Locate every blood parasite and identify its species.
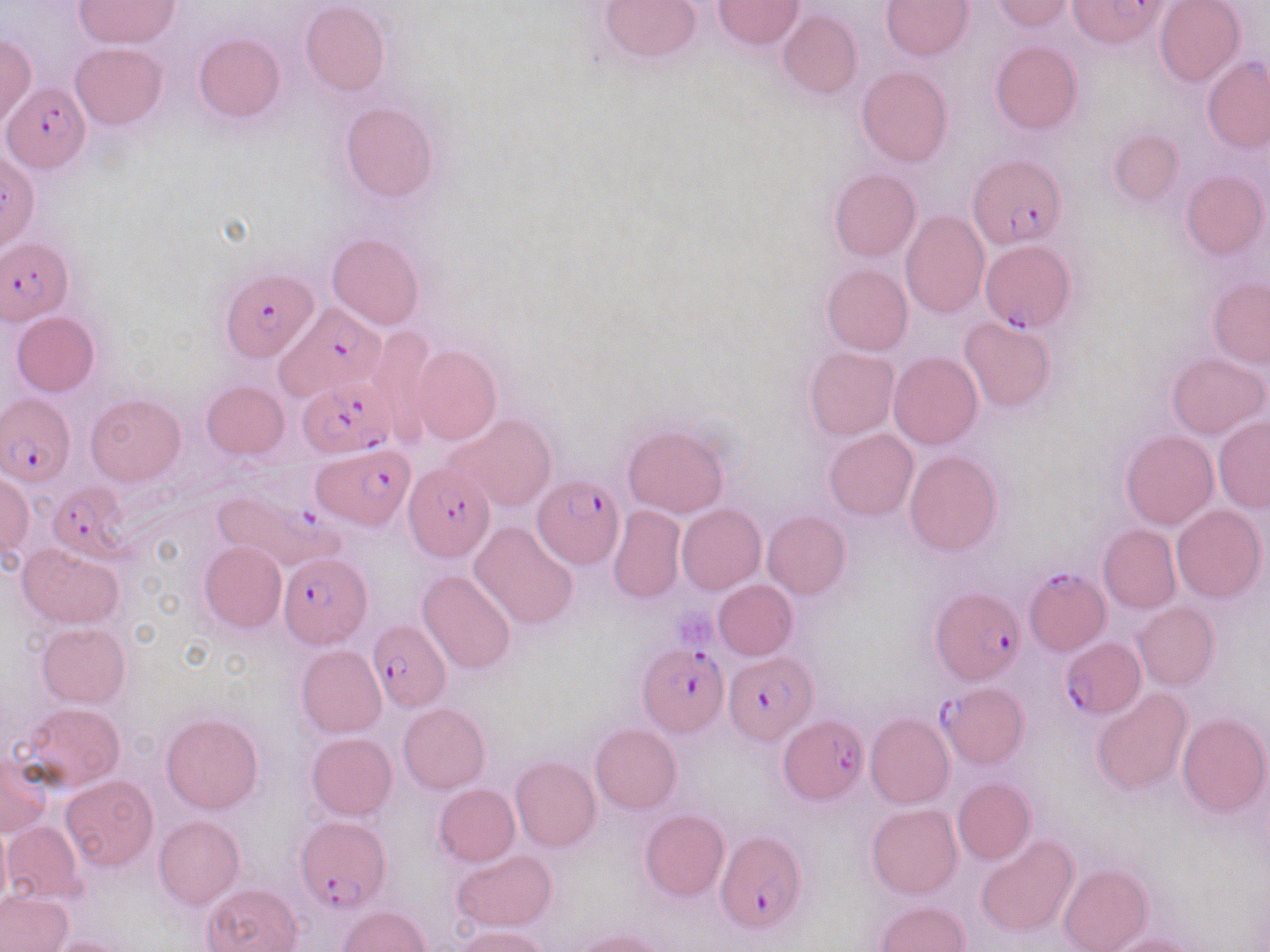
Approximate bounding boxes as [x1, y1, x2, y2] in pixels.
Plasmodium falciparum-infected red blood cells: [1068, 0, 1169, 46], [5, 81, 89, 174], [968, 151, 1067, 251], [0, 238, 74, 323], [980, 240, 1075, 331], [221, 269, 317, 360], [271, 304, 384, 400], [297, 378, 396, 457], [3, 393, 75, 485], [314, 445, 414, 531], [404, 463, 495, 563], [532, 474, 622, 572], [45, 483, 126, 561], [211, 487, 340, 575], [278, 552, 370, 648], [1024, 569, 1108, 657], [930, 587, 1023, 687], [368, 620, 452, 712], [1061, 637, 1146, 718], [639, 643, 728, 739], [723, 652, 813, 745], [938, 683, 1029, 768], [779, 715, 866, 801], [294, 815, 390, 911], [714, 830, 806, 936].
No Plasmodium ovale, Plasmodium malariae, Plasmodium vivax, Babesia divergens, or Trypanosoma brucei observed.

Platelet locations: [674, 604, 720, 653]. Uninfected red blood cell locations: [74, 0, 180, 48], [599, 0, 703, 65], [881, 0, 972, 59], [991, 0, 1073, 32], [301, 1, 390, 96], [712, 1, 804, 49], [1154, 1, 1244, 86], [778, 9, 861, 99], [194, 32, 285, 121], [0, 34, 36, 127], [989, 41, 1082, 134], [71, 42, 166, 131], [1203, 57, 1270, 151], [856, 67, 952, 166], [341, 101, 439, 202], [1108, 129, 1183, 206], [828, 169, 921, 262], [1181, 171, 1268, 260], [900, 210, 989, 319], [327, 233, 424, 331], [822, 264, 913, 355], [1208, 276, 1270, 368], [11, 312, 101, 396], [958, 316, 1057, 411], [368, 327, 436, 442], [410, 344, 501, 445], [803, 346, 900, 441], [888, 352, 982, 449], [1165, 352, 1267, 439], [200, 380, 289, 459], [86, 393, 185, 486], [447, 414, 556, 511], [1214, 416, 1270, 512], [622, 424, 729, 518], [824, 430, 918, 520], [1121, 431, 1219, 530], [904, 451, 1002, 555], [0, 473, 33, 559], [1171, 504, 1264, 602], [676, 505, 765, 594], [606, 506, 685, 603], [762, 510, 850, 598], [470, 521, 578, 630], [1098, 524, 1179, 613], [199, 541, 286, 633], [17, 544, 124, 627], [417, 569, 518, 677], [713, 579, 798, 660], [1133, 602, 1219, 691], [37, 621, 129, 707], [295, 646, 387, 738], [1092, 688, 1192, 795], [19, 702, 126, 792], [398, 703, 489, 794], [161, 713, 263, 814], [864, 713, 954, 810], [1177, 713, 1269, 817], [591, 723, 682, 814], [305, 733, 397, 821], [0, 754, 52, 838], [510, 757, 602, 852], [61, 776, 158, 870], [953, 779, 1036, 864], [434, 784, 520, 866], [866, 803, 962, 898], [640, 809, 729, 900], [153, 815, 243, 910], [3, 821, 86, 904], [0, 823, 10, 911], [975, 834, 1078, 937], [451, 851, 558, 932], [1058, 864, 1153, 952], [203, 882, 302, 952], [0, 890, 72, 952], [875, 900, 969, 952], [339, 906, 429, 951], [453, 926, 551, 952], [571, 929, 674, 952], [1103, 934, 1199, 952], [45, 936, 134, 952]. Slide-level diagnosis: Plasmodium falciparum. Image is 1270×952 pixels. May-Grünwald-Giemsa stain. Thin blood film. 1000x magnification. Light microscopy. Single field of view.